State which cell type is depicted.
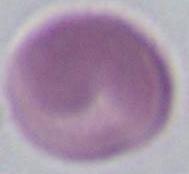
This is an erythrocyte.

Micrograph. 1000x magnification.